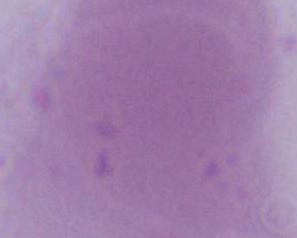

Summary:
  - Modality: micrograph
  - Magnification: 1000x
  - Identification: red blood cell